Classify this cell by malaria status.
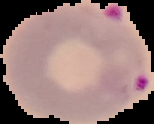
Parasitized.

{
  "image_type": "segmented cell region on a black background",
  "preparation": "thin blood film",
  "image_size": "154×124 pixels"
}